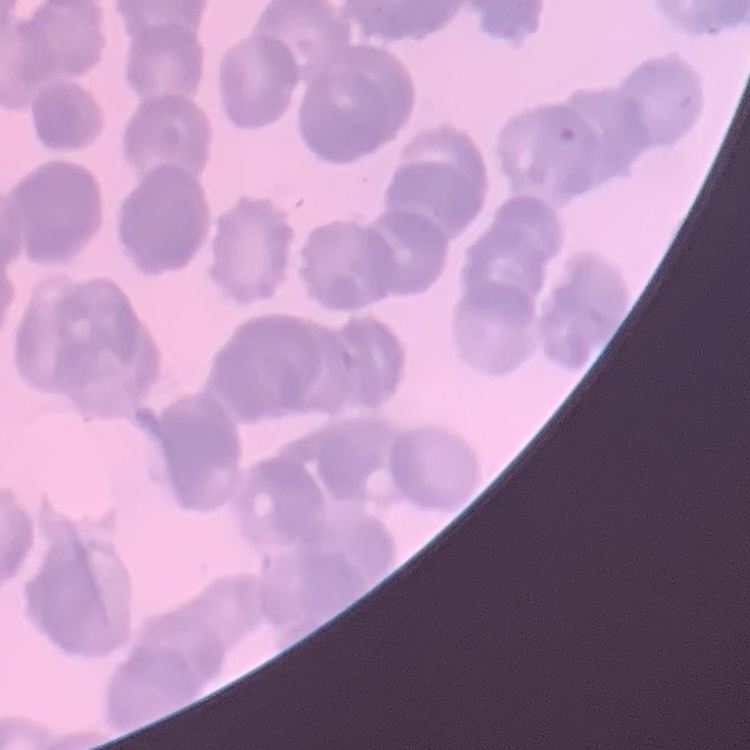

erythrocyte morphology = rouleaux formation
stain = Field's or Giemsa
preparation = thin blood film
image type = square crop of a larger photomicrograph